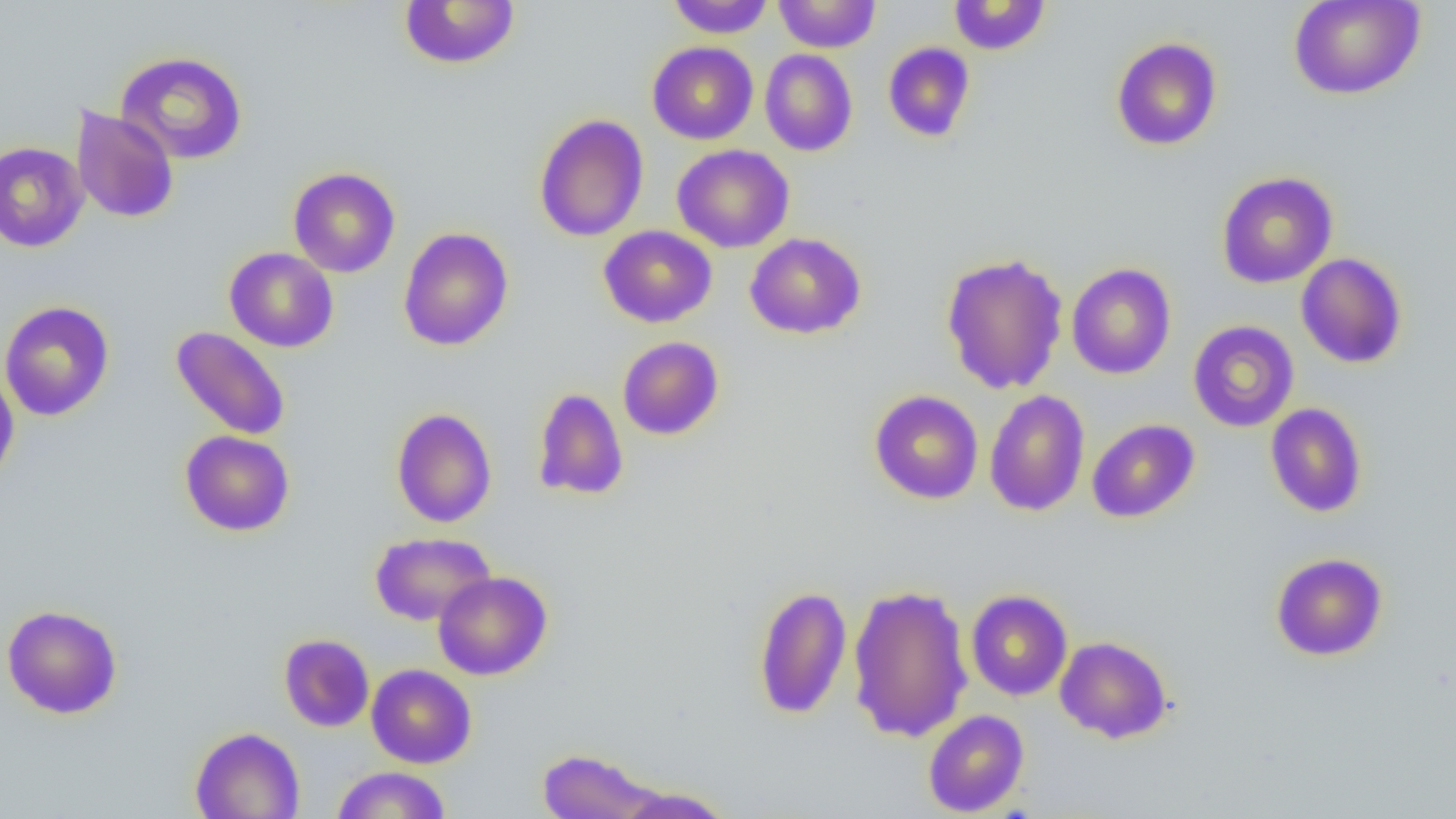

Summary:
  - Coordinate format: approximate bounding boxes as [x1, y1, x2, y2] in pixels
  - Uninfected red blood cell locations: [667, 0, 774, 38], [774, 0, 881, 53], [949, 0, 1050, 55], [1288, 0, 1426, 100], [399, 1, 520, 70], [1111, 37, 1223, 151], [647, 41, 758, 145], [882, 41, 976, 142], [760, 49, 858, 156], [115, 51, 248, 164], [71, 105, 180, 223], [533, 113, 649, 242], [0, 141, 89, 252], [671, 144, 795, 253], [288, 167, 400, 278], [1216, 172, 1337, 288], [598, 225, 717, 328], [398, 227, 513, 351], [744, 233, 866, 339], [225, 247, 338, 352], [940, 251, 1069, 394], [1296, 253, 1408, 369], [1066, 262, 1176, 379], [0, 300, 114, 421], [1187, 320, 1299, 432], [170, 326, 291, 440], [617, 336, 724, 440], [0, 370, 20, 488], [532, 387, 629, 501], [869, 390, 983, 504], [984, 390, 1090, 516], [1265, 403, 1368, 518], [391, 408, 497, 528], [1087, 418, 1200, 523], [179, 430, 294, 536], [370, 532, 496, 626], [1270, 552, 1388, 661], [433, 571, 552, 680], [847, 583, 974, 743], [754, 585, 852, 720], [965, 590, 1073, 700], [2, 604, 123, 719], [279, 633, 375, 732], [1054, 635, 1173, 744], [366, 664, 477, 768], [923, 709, 1029, 817], [190, 726, 305, 819], [537, 748, 661, 818], [331, 766, 451, 819], [614, 785, 735, 818]
  - Slide-level diagnosis: negative for blood parasites
  - Image size: 1456×819 pixels
  - Preparation: thin blood smear
  - Magnification: 1000x
  - Field of view: one of a larger specimen
  - Modality: light microscopy